Locate and identify every blood parasite.
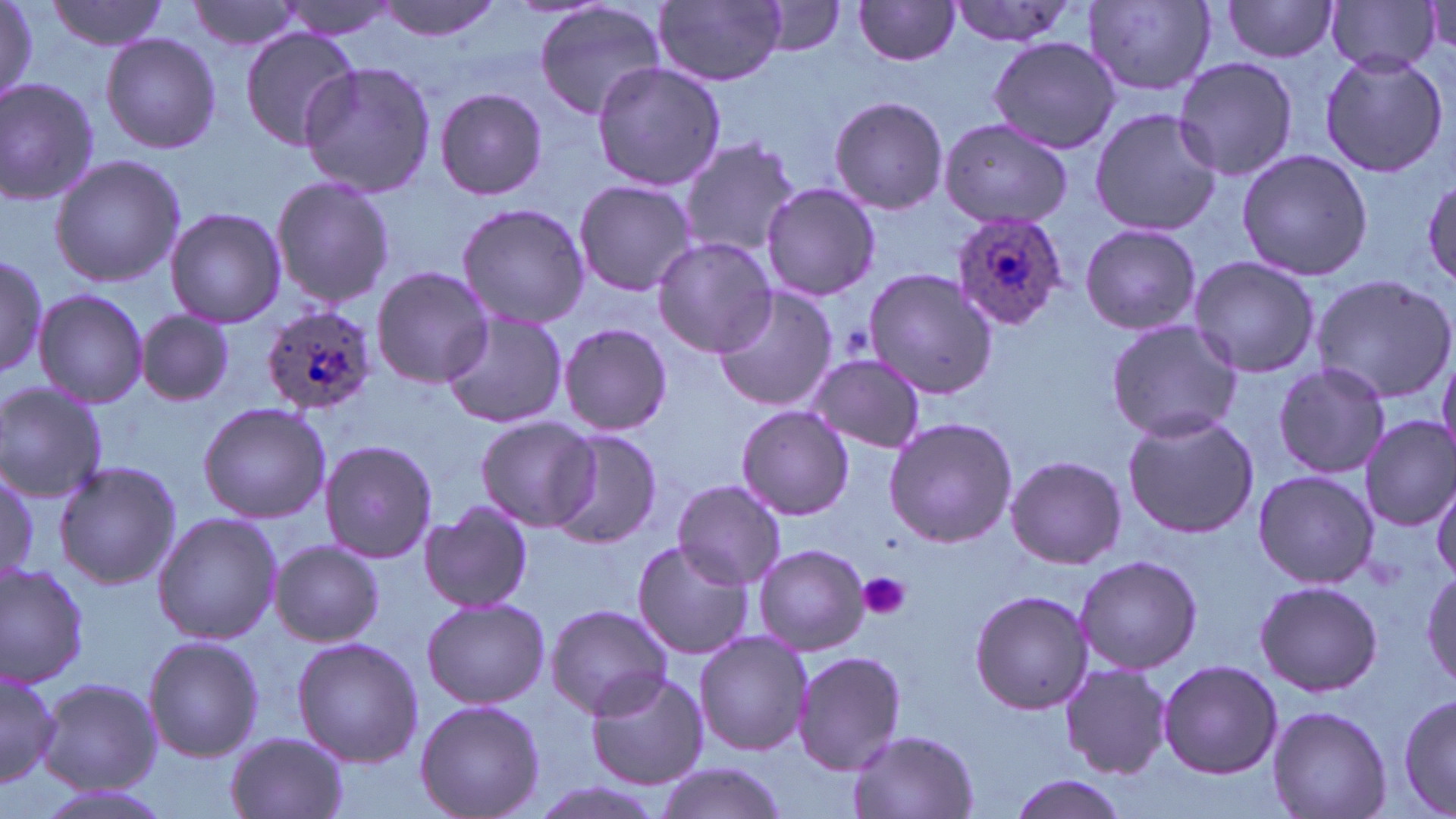

Approximate bounding boxes as (x1, y1, x2, y2) in pixels.
Plasmodium ovale-infected red blood cells: (952, 209, 1068, 331), (258, 303, 377, 416).
No Plasmodium falciparum, Plasmodium malariae, Plasmodium vivax, Babesia divergens, or Trypanosoma brucei observed.

Uninfected red blood cell locations: (0, 0, 46, 108), (45, 0, 172, 52), (186, 0, 306, 53), (276, 0, 403, 39), (373, 0, 507, 41), (656, 1, 787, 86), (1222, 1, 1341, 61), (534, 2, 668, 123), (853, 2, 964, 66), (943, 2, 1080, 47), (1086, 2, 1215, 95), (1326, 2, 1440, 73), (759, 3, 848, 56), (238, 27, 364, 150), (100, 32, 221, 154), (987, 36, 1121, 155), (1317, 52, 1449, 177), (1172, 56, 1299, 182), (299, 61, 438, 198), (591, 62, 727, 191), (0, 77, 101, 206), (433, 88, 548, 201), (828, 96, 949, 214), (1089, 107, 1221, 237), (939, 118, 1073, 231), (677, 136, 801, 257), (1235, 148, 1374, 282), (49, 154, 187, 287), (270, 174, 396, 309), (1422, 175, 1456, 287), (573, 178, 697, 298), (761, 181, 880, 301), (456, 202, 590, 330), (164, 206, 286, 329), (1079, 223, 1202, 337), (650, 236, 776, 356), (0, 247, 46, 381), (1188, 255, 1320, 379), (370, 266, 493, 388), (864, 269, 997, 400), (1312, 274, 1456, 404), (712, 284, 838, 412), (33, 289, 149, 407), (136, 310, 233, 407), (438, 310, 570, 429), (1105, 319, 1244, 442), (557, 322, 673, 436), (1436, 346, 1456, 462), (806, 353, 926, 452), (1272, 360, 1391, 482), (0, 382, 107, 500), (197, 401, 332, 523), (736, 405, 854, 520), (1120, 410, 1259, 539), (475, 415, 596, 531), (1357, 415, 1456, 530), (885, 417, 1018, 547), (544, 427, 663, 548), (319, 440, 439, 564), (1003, 453, 1127, 569), (53, 459, 182, 591), (1, 467, 41, 584), (1251, 470, 1380, 590), (1430, 478, 1456, 581), (671, 479, 789, 588), (416, 501, 537, 612), (152, 510, 282, 645), (630, 539, 756, 663), (269, 540, 387, 646), (752, 543, 870, 656), (1073, 554, 1204, 674), (0, 561, 91, 687), (1421, 569, 1456, 693), (1253, 579, 1385, 698), (968, 589, 1095, 716), (421, 597, 550, 710), (543, 604, 673, 718), (693, 629, 812, 757), (292, 635, 423, 766), (143, 636, 263, 762), (791, 648, 909, 776), (1158, 659, 1282, 779), (1059, 663, 1172, 780), (1, 664, 61, 791), (583, 670, 710, 789), (38, 677, 160, 794), (1394, 688, 1454, 819), (413, 699, 545, 819), (1265, 705, 1392, 819), (847, 729, 978, 819), (225, 731, 351, 819), (652, 760, 789, 819), (1004, 774, 1131, 819). Platelet locations: (841, 327, 872, 363), (858, 573, 910, 621). Slide-level diagnosis: Plasmodium ovale. May-Grünwald-Giemsa stain. Single field of view. Light microscopy. Image is 1456×819 pixels. 1000x magnification. Thin blood smear.